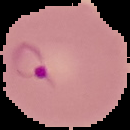
image size = 130×130 pixels
preparation = thin blood smear
image type = cell region segmented out of the field of view; surrounding area masked to black
malaria status = parasitized